Comment on the morphology of the erythrocytes.
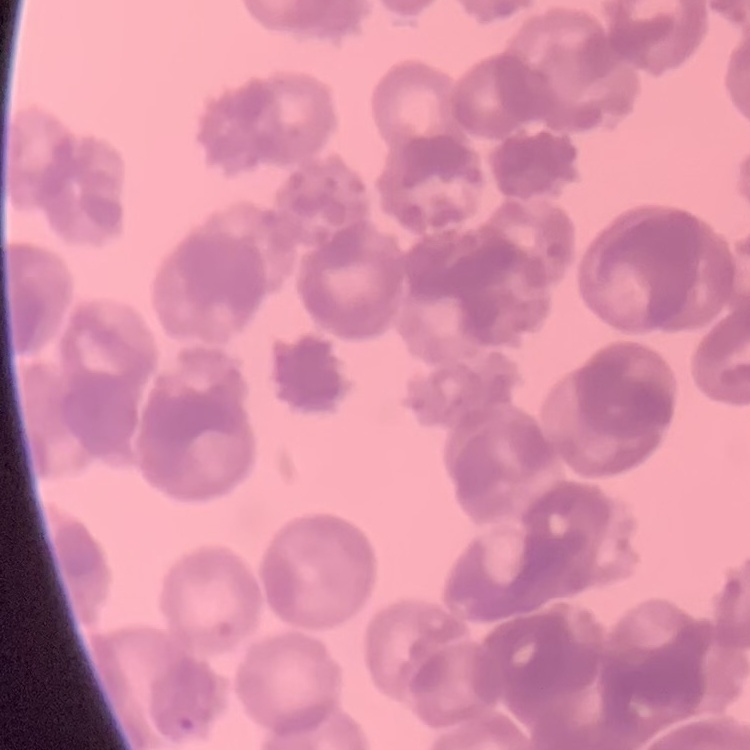
Rouleaux formation.

preparation = thin peripheral smear
stain = Field's or Giemsa
image type = one tile cut from a larger photomicrograph